Assess this cell for malaria.
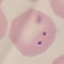

Parasitized.

Automatically extracted cell patch, resized to 64 × 64 pixels. Giemsa stain. Photographed with a smartphone camera at the microscope eyepiece. Thin smear of blood.